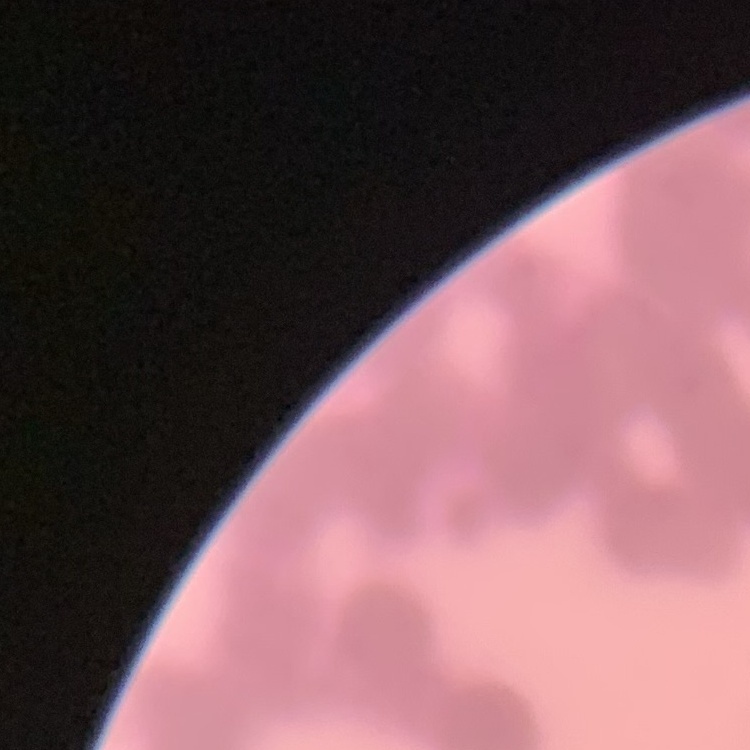
The red blood cells show rouleaux formation. Thin blood smear. Square crop of a larger photomicrograph. Stained with either Field's or Giemsa.